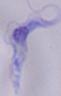

Summary:
  - Magnification: 1000x
  - Identification: trypanosome
  - Modality: photomicrograph